Identify the parasite.
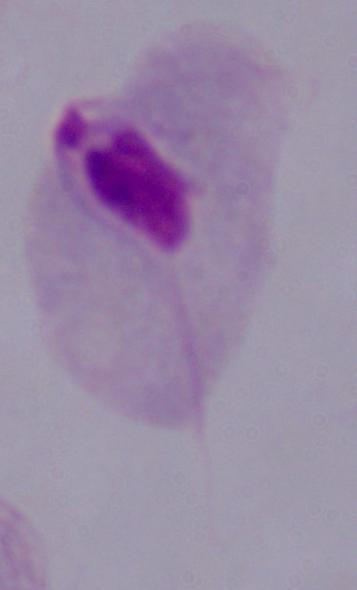

A trichomonad.

modality = photomicrograph
magnification = 1000x